Assess this cell for malaria.
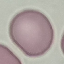

Uninfected.

Giemsa-stained preparation. Cell patch, automatically extracted from a larger field of view and resized to 64 × 64 pixels. Thin blood smear. Photographed with a smartphone camera at the microscope eyepiece.